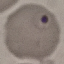

{
  "malaria_status": "parasitized",
  "preparation": "thin blood film",
  "capture": "smartphone camera at the microscope eyepiece",
  "stain": "Giemsa",
  "image_type": "cell patch, automatically extracted from a larger field of view and resized to 64 × 64 pixels"
}